Identify the parasite.
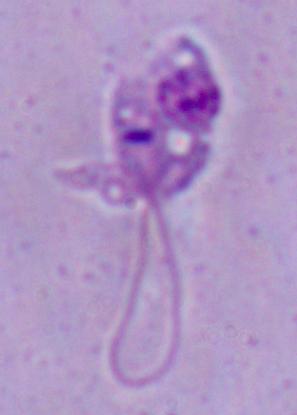
Leishmania.

1000x magnification. Micrograph.